Locate and identify every blood parasite.
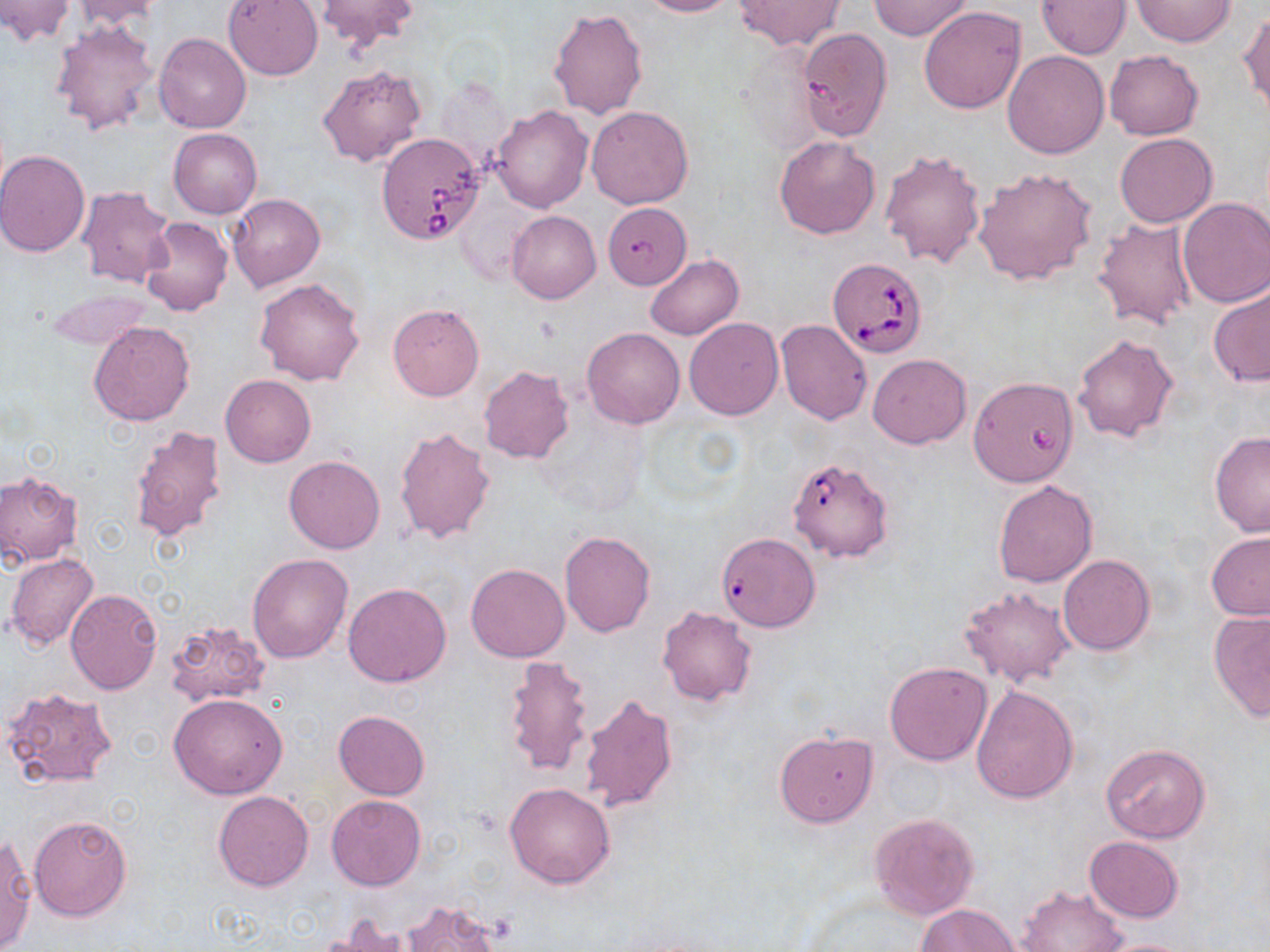

Approximate bounding boxes as [x1, y1, x2, y2] in pixels.
Babesia divergens-infected red blood cells: [376, 132, 486, 243], [822, 259, 927, 362], [787, 456, 894, 562], [719, 537, 819, 634].
No Plasmodium falciparum, Plasmodium ovale, Plasmodium malariae, Plasmodium vivax, or Trypanosoma brucei observed.

Summary:
  - Uninfected red blood cell locations: [0, 0, 75, 44], [67, 0, 164, 32], [223, 0, 323, 81], [313, 0, 421, 50], [639, 0, 738, 16], [734, 0, 844, 49], [870, 0, 974, 40], [1036, 0, 1131, 59], [1131, 0, 1236, 47], [919, 6, 1026, 114], [548, 7, 647, 120], [1239, 10, 1269, 116], [51, 19, 158, 134], [806, 30, 890, 141], [154, 32, 251, 133], [1002, 50, 1110, 159], [1105, 51, 1204, 140], [319, 64, 427, 167], [491, 104, 594, 212], [585, 105, 694, 209], [169, 128, 262, 219], [1115, 133, 1217, 227], [773, 135, 880, 240], [880, 148, 986, 269], [0, 149, 91, 256], [972, 168, 1098, 286], [77, 184, 174, 288], [229, 193, 325, 291], [1177, 198, 1270, 307], [603, 203, 694, 287], [507, 210, 600, 303], [1093, 216, 1199, 332], [142, 218, 233, 317], [645, 254, 743, 340], [255, 277, 365, 385], [1208, 283, 1270, 388], [46, 287, 155, 352], [388, 303, 485, 401], [684, 318, 784, 420], [776, 320, 872, 425], [89, 321, 194, 426], [581, 328, 685, 429], [1072, 332, 1180, 443], [867, 353, 971, 448], [478, 365, 574, 463], [221, 374, 316, 467], [970, 377, 1076, 488], [128, 425, 227, 543], [394, 425, 495, 544], [1209, 431, 1270, 539], [284, 455, 385, 553], [0, 471, 83, 566], [992, 480, 1097, 588], [559, 529, 655, 637], [1205, 532, 1270, 621], [5, 553, 100, 650], [246, 553, 355, 663], [1058, 555, 1156, 656], [31, 563, 137, 685], [466, 563, 569, 663], [343, 583, 451, 687], [960, 584, 1075, 688], [65, 587, 163, 694], [658, 605, 757, 706], [1208, 609, 1270, 721], [163, 619, 273, 709], [502, 655, 595, 779], [885, 661, 992, 766], [970, 685, 1079, 803], [3, 686, 117, 791], [579, 692, 678, 814], [168, 693, 288, 799], [334, 711, 430, 800], [774, 730, 878, 828], [1101, 743, 1211, 842], [504, 782, 616, 888], [213, 791, 314, 891], [326, 795, 426, 891], [868, 812, 980, 921], [28, 814, 132, 922], [0, 835, 34, 951], [1084, 836, 1183, 924], [1016, 883, 1129, 952], [399, 898, 502, 952], [918, 903, 1021, 952], [321, 915, 418, 952], [1100, 938, 1195, 952]
  - Slide-level diagnosis: Babesia divergens
  - Stain: May-Grünwald-Giemsa
  - Preparation: thin blood smear
  - Image size: 1270×952 pixels
  - Magnification: 1000x
  - Field of view: single
  - Modality: light microscopy